Assess the morphology of the erythrocytes.
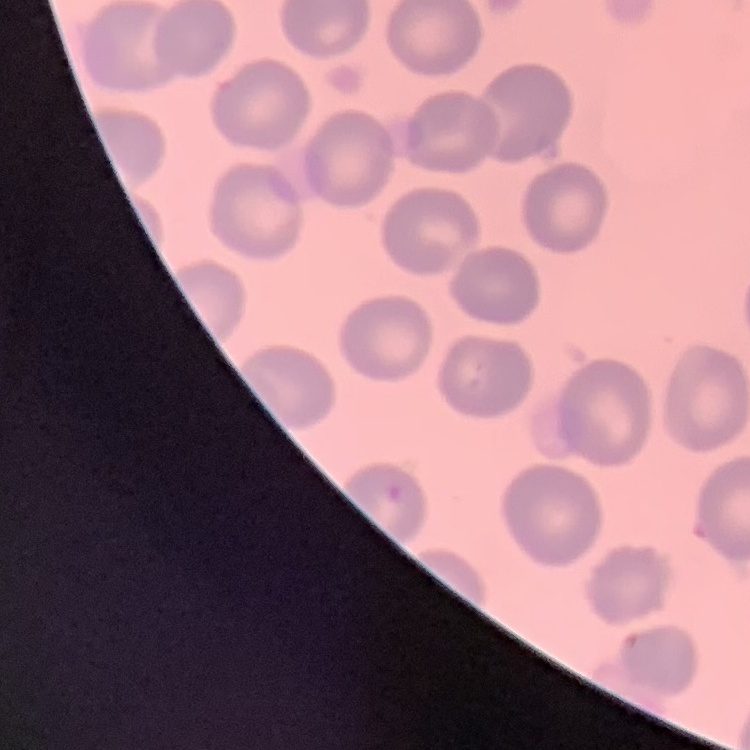
They show no rouleaux formation.

Thin blood smear. Field's or Giemsa stain. Square crop of a larger photomicrograph.